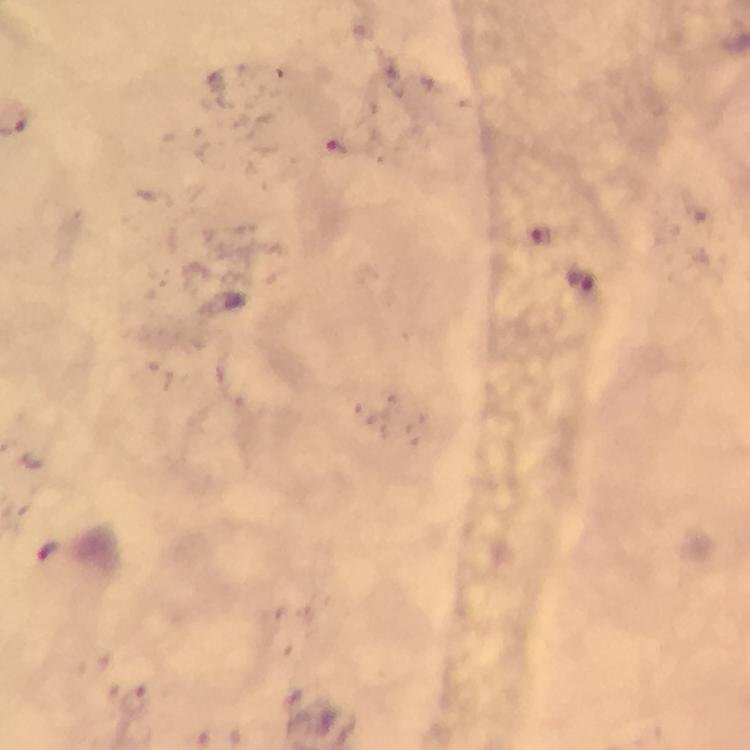
Approximate object centers, in pixels from the top-left corner.
Summary:
  - Malaria parasite locations: (x=338, y=149), (x=49, y=549), (x=136, y=702)
  - Image size: 750×750 pixels
  - Stain: Giemsa
  - Cropped from: one field of view
  - Context: from a malaria diagnostic workup
  - Magnification: 100x
  - Capture: smartphone camera through the microscope
  - Immersion oil: used
  - Preparation: thick blood smear